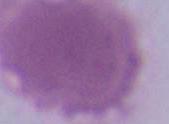

A red blood cell is seen. 1000x magnification. Photomicrograph.